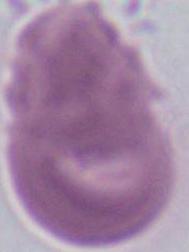

Summary:
  - Identification: erythrocyte
  - Modality: photomicrograph
  - Magnification: 1000x